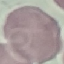

Summary:
  - Result: no malaria parasites seen
  - Stain: Giemsa
  - Preparation: thin blood film
  - Image type: automatically extracted cell patch, resized to 64 × 64 pixels
  - Capture: smartphone through the microscope eyepiece